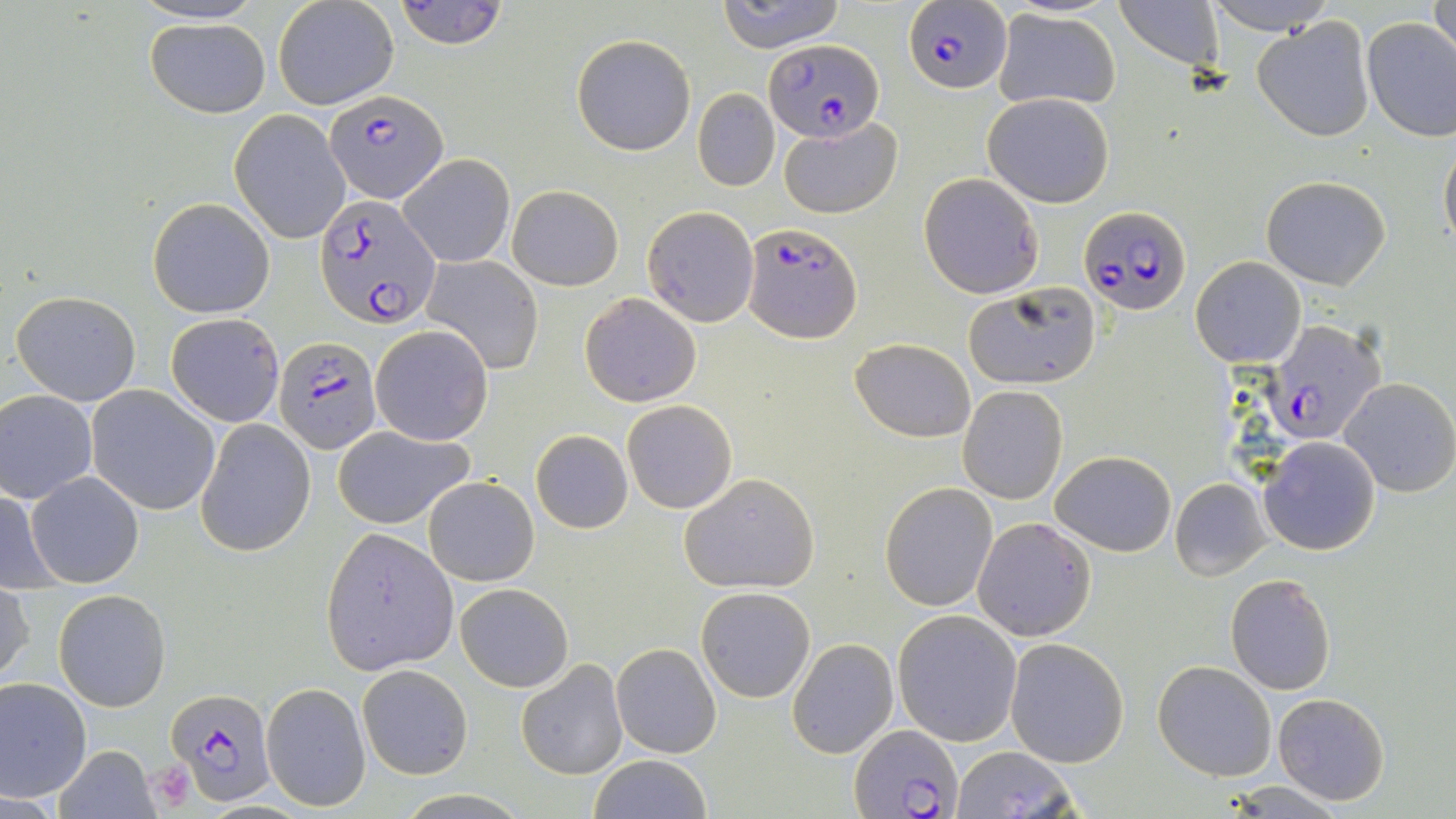

{
  "slide_level_diagnosis": "Plasmodium falciparum",
  "field_of_view": "single",
  "magnification": "1000x",
  "modality": "light microscopy",
  "image_size": "1456×819 pixels",
  "uninfected_red_blood_cell_locations_subset": "approximate bounding boxes as named x1/y1/x2/y2 corners in pixels: (x1=393, y1=0, x2=509, y2=49), (x1=718, y1=0, x2=847, y2=53), (x1=1207, y1=0, x2=1329, y2=31), (x1=1429, y1=0, x2=1455, y2=66), (x1=272, y1=1, x2=399, y2=110), (x1=1116, y1=1, x2=1227, y2=72), (x1=993, y1=8, x2=1121, y2=111), (x1=1252, y1=15, x2=1375, y2=143), (x1=145, y1=17, x2=272, y2=117), (x1=1361, y1=17, x2=1456, y2=141), (x1=571, y1=33, x2=695, y2=155), (x1=693, y1=89, x2=779, y2=191), (x1=983, y1=92, x2=1115, y2=208), (x1=229, y1=109, x2=351, y2=244), (x1=778, y1=116, x2=904, y2=221), (x1=1439, y1=137, x2=1456, y2=252), (x1=398, y1=153, x2=515, y2=268), (x1=918, y1=173, x2=1042, y2=298), (x1=1262, y1=175, x2=1391, y2=289), (x1=507, y1=184, x2=625, y2=292), (x1=147, y1=197, x2=275, y2=318), (x1=641, y1=205, x2=759, y2=326), (x1=422, y1=254, x2=544, y2=373), (x1=1192, y1=257, x2=1304, y2=368), (x1=962, y1=281, x2=1102, y2=387), (x1=10, y1=289, x2=142, y2=406), (x1=579, y1=292, x2=701, y2=407), (x1=164, y1=313, x2=286, y2=426), (x1=370, y1=325, x2=493, y2=445), (x1=850, y1=337, x2=977, y2=441), (x1=1338, y1=378, x2=1455, y2=496), (x1=957, y1=384, x2=1068, y2=504), (x1=86, y1=385, x2=220, y2=515), (x1=0, y1=390, x2=98, y2=501), (x1=622, y1=400, x2=737, y2=513), (x1=195, y1=419, x2=317, y2=557), (x1=332, y1=425, x2=476, y2=529), (x1=529, y1=430, x2=630, y2=529), (x1=1258, y1=437, x2=1380, y2=554), (x1=1050, y1=449, x2=1176, y2=557), (x1=23, y1=470, x2=144, y2=589), (x1=679, y1=472, x2=820, y2=594), (x1=423, y1=475, x2=538, y2=587), (x1=1170, y1=478, x2=1271, y2=581), (x1=880, y1=481, x2=998, y2=611), (x1=0, y1=489, x2=59, y2=590), (x1=972, y1=517, x2=1096, y2=642), (x1=319, y1=528, x2=458, y2=672), (x1=1225, y1=574, x2=1336, y2=695), (x1=0, y1=580, x2=34, y2=689), (x1=454, y1=581, x2=574, y2=692), (x1=696, y1=586, x2=814, y2=703), (x1=54, y1=590, x2=170, y2=711), (x1=893, y1=611, x2=1022, y2=745), (x1=1005, y1=637, x2=1130, y2=768), (x1=788, y1=638, x2=898, y2=758), (x1=612, y1=643, x2=720, y2=757), (x1=516, y1=658, x2=629, y2=777), (x1=1152, y1=660, x2=1276, y2=781), (x1=357, y1=664, x2=472, y2=780), (x1=0, y1=677, x2=93, y2=800), (x1=261, y1=682, x2=370, y2=812), (x1=1272, y1=693, x2=1392, y2=806), (x1=55, y1=744, x2=158, y2=818), (x1=949, y1=746, x2=1083, y2=819), (x1=585, y1=755, x2=712, y2=818), (x1=1224, y1=781, x2=1347, y2=815)",
  "preparation": "thin blood smear",
  "stain": "May-Grünwald-Giemsa",
  "platelet_locations": "approximate bounding boxes as named x1/y1/x2/y2 corners in pixels: (x1=147, y1=759, x2=195, y2=806)",
  "plasmodium_falciparum_infected_red_blood_cell_locations_subset": "approximate bounding boxes as named x1/y1/x2/y2 corners in pixels: (x1=903, y1=2, x2=1013, y2=94), (x1=761, y1=38, x2=883, y2=141), (x1=325, y1=89, x2=447, y2=201), (x1=312, y1=195, x2=440, y2=327), (x1=1081, y1=203, x2=1190, y2=314), (x1=741, y1=222, x2=862, y2=345), (x1=273, y1=335, x2=385, y2=454), (x1=166, y1=688, x2=278, y2=805), (x1=850, y1=724, x2=963, y2=818)"
}